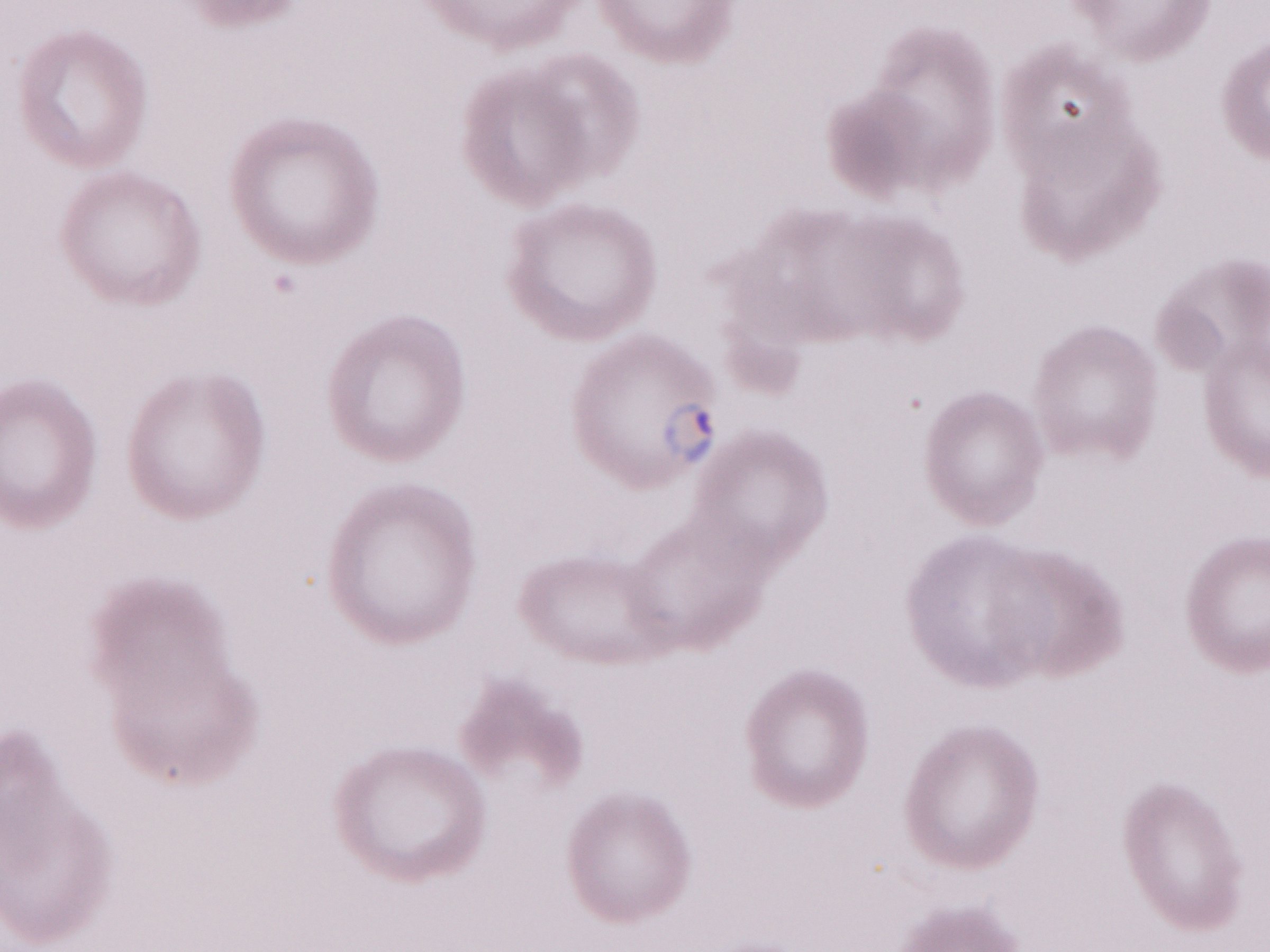

Image is 1270×952 pixels. Olympus BX43 microscope, Olympus DP73 camera. 1,000x magnification. Thin blood smear. One field of this slide. May-Grünwald-Giemsa (MGG) stain. Malaria diagnosis (patient-level): positive.